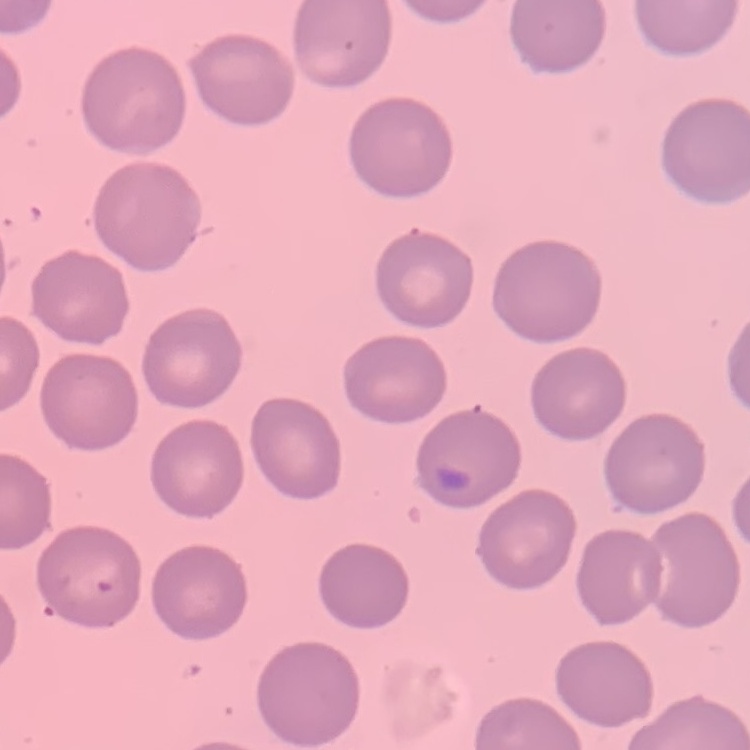
Summary:
  - Red blood cell morphology: no rouleaux formation
  - Stain: Field's or Giemsa
  - Preparation: thin blood film
  - Image type: one tile cut from a larger photomicrograph